State the preparation type.
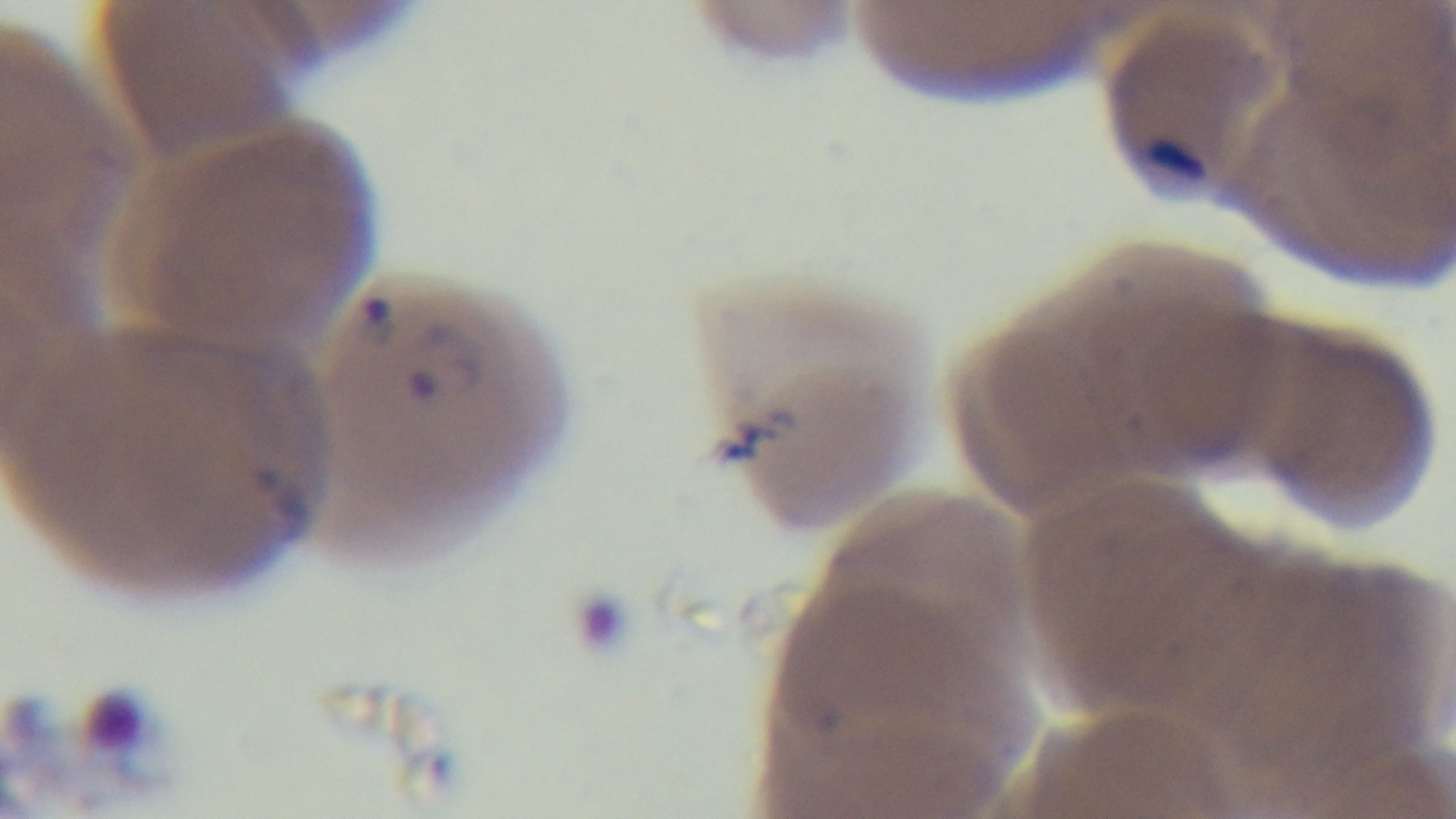

Thin.

Summary:
  - Stain: Giemsa
  - Field of view: one from the slide
  - Malaria status: infected
  - Capture: mounted 4K digital camera
  - Objective: 100x oil immersion
  - Modality: light microscopy